Give the preparation type.
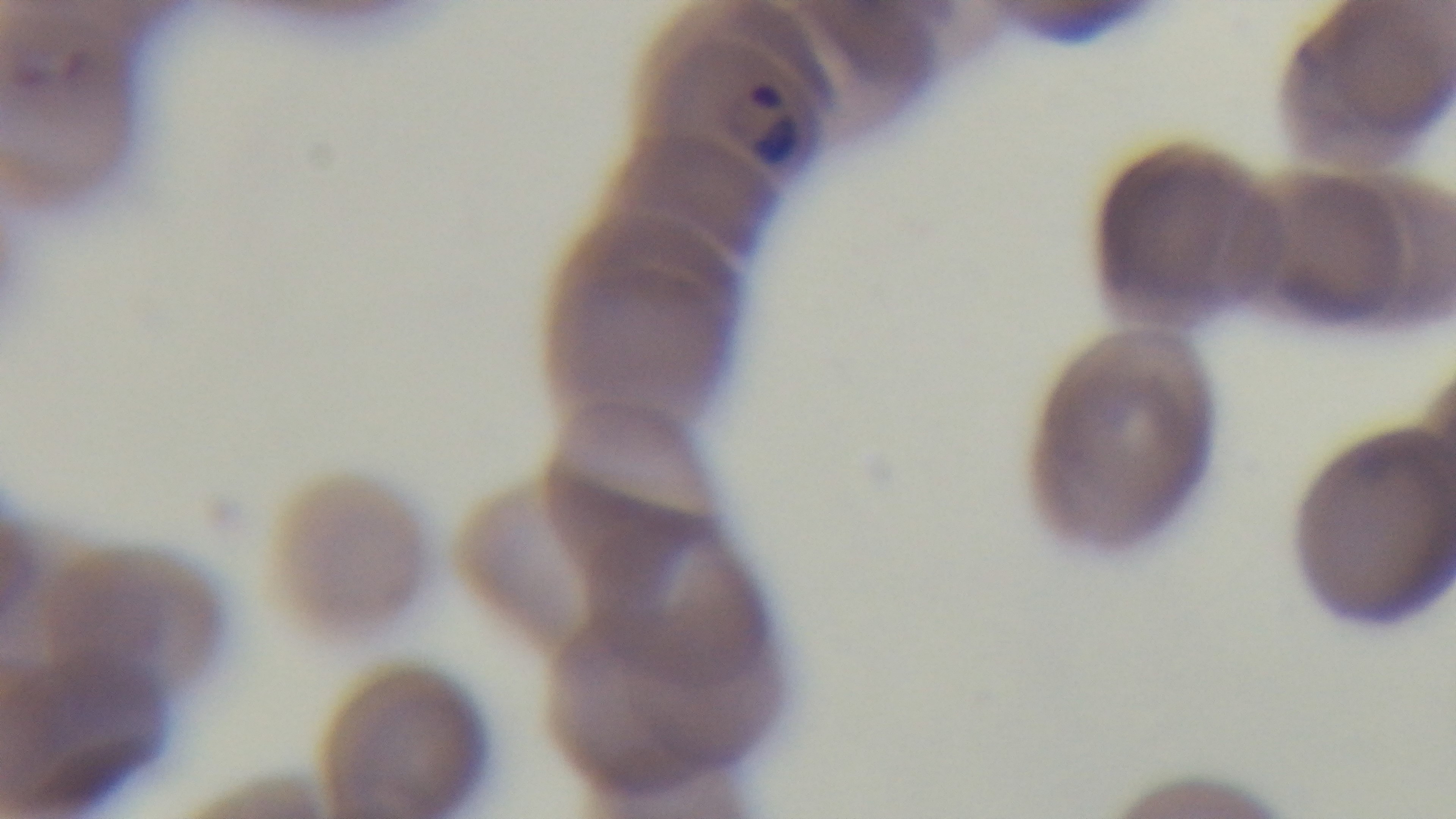
It is a thin blood film.

capture = mounted 4K digital camera
stain = Giemsa
malaria status = infected
field of view = single
modality = light microscopy
objective = 100x oil immersion